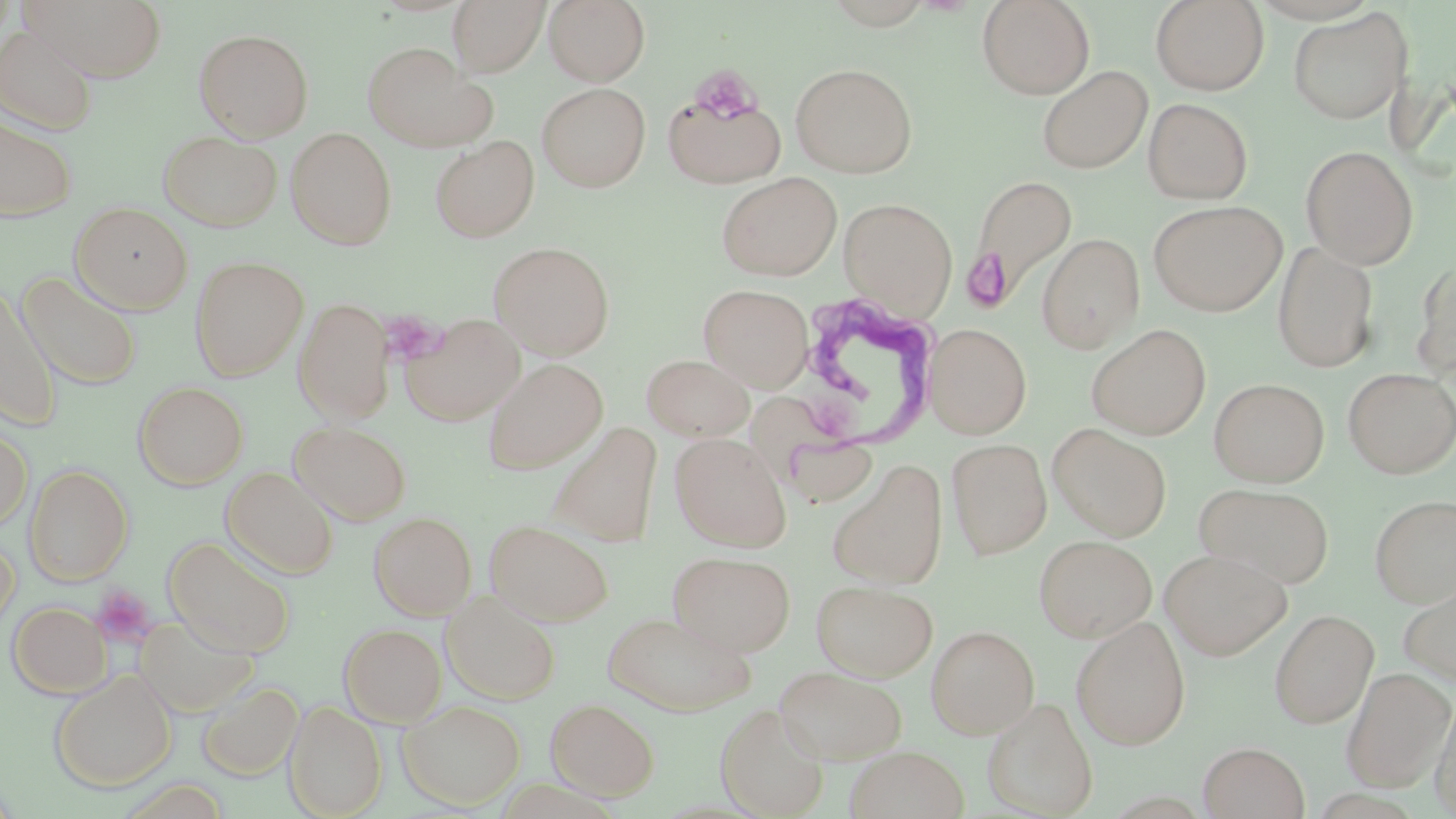
Approximate bounding boxes as (x1, y1, x2, y2) in pixels. Platelet locations: (698, 69, 768, 124), (968, 251, 1016, 306), (390, 312, 452, 359), (90, 585, 157, 649). Trypanosoma brucei locations: (790, 291, 944, 452). Uninfected red blood cell locations: (23, 0, 168, 82), (448, 0, 549, 76), (544, 0, 650, 86), (976, 0, 1095, 99), (1150, 0, 1269, 96), (1288, 8, 1412, 125), (0, 24, 98, 135), (193, 28, 314, 142), (362, 41, 495, 152), (790, 63, 918, 178), (1036, 65, 1153, 175), (536, 82, 651, 192), (662, 88, 786, 188), (1143, 97, 1253, 204), (0, 115, 77, 221), (285, 127, 397, 249), (158, 129, 282, 232), (430, 136, 539, 243), (1300, 145, 1418, 269), (716, 172, 843, 281), (969, 173, 1078, 304), (838, 197, 958, 318), (1148, 200, 1287, 316), (70, 201, 193, 314), (1036, 233, 1144, 352), (488, 241, 615, 359), (1272, 241, 1379, 373), (189, 255, 309, 381), (1413, 256, 1456, 380), (17, 271, 142, 391), (698, 284, 814, 392), (1, 285, 60, 429), (294, 297, 394, 424), (399, 312, 526, 425), (925, 323, 1032, 438), (1086, 323, 1211, 440), (642, 354, 755, 441), (482, 358, 608, 474), (1343, 367, 1456, 478), (1209, 378, 1329, 487), (133, 381, 248, 490), (289, 420, 411, 525), (0, 421, 32, 532), (547, 422, 664, 547), (1047, 423, 1172, 541), (670, 433, 792, 552), (947, 439, 1052, 559), (827, 459, 948, 590), (24, 464, 132, 585), (221, 466, 339, 579), (1194, 482, 1336, 588), (1369, 494, 1456, 608), (368, 511, 476, 620), (484, 518, 614, 626), (1034, 534, 1157, 642), (0, 535, 20, 639), (164, 536, 296, 657), (1159, 548, 1292, 661), (668, 550, 795, 656), (1397, 574, 1456, 685), (811, 580, 938, 681), (441, 591, 561, 705), (8, 601, 111, 698), (1269, 608, 1379, 728), (602, 610, 756, 716), (133, 614, 258, 718), (1071, 616, 1191, 750), (339, 623, 447, 726), (926, 625, 1039, 739), (774, 665, 908, 764), (1341, 668, 1455, 792), (50, 670, 176, 792), (198, 680, 303, 780), (1430, 693, 1456, 817), (982, 696, 1098, 817), (546, 697, 658, 800), (397, 699, 526, 810), (284, 700, 387, 818), (715, 702, 830, 818), (1198, 741, 1310, 819), (844, 746, 970, 819). Slide-level diagnosis: Trypanosoma brucei. Image is 1456×819 pixels. May-Grünwald-Giemsa stain. Thin blood film. Captured at 1000x magnification. Single field of view. Light microscopy.